State which parasite is depicted.
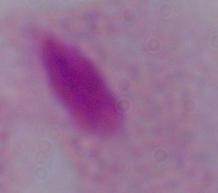
This is a trichomonad.

modality = photomicrograph
magnification = 1000x